State the preparation type.
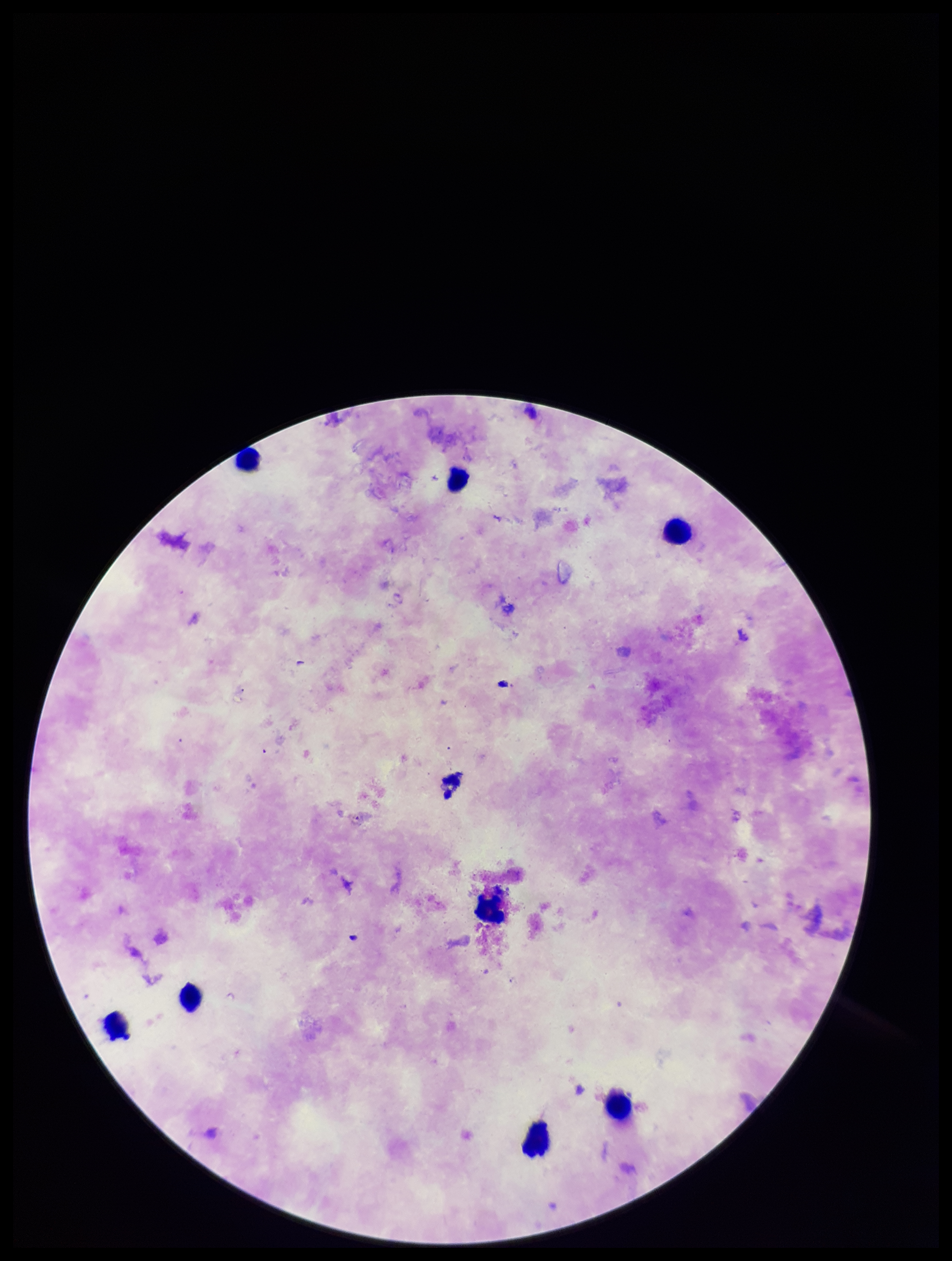

A thick smear.

field of view = one from this slide
Plasmodium parasites = none seen
stain = Giemsa
leukocyte count = 8
capture = smartphone photograph through the microscope eyepiece
image size = 952×1261 pixels
parasite count = 0
patient malaria status = negative